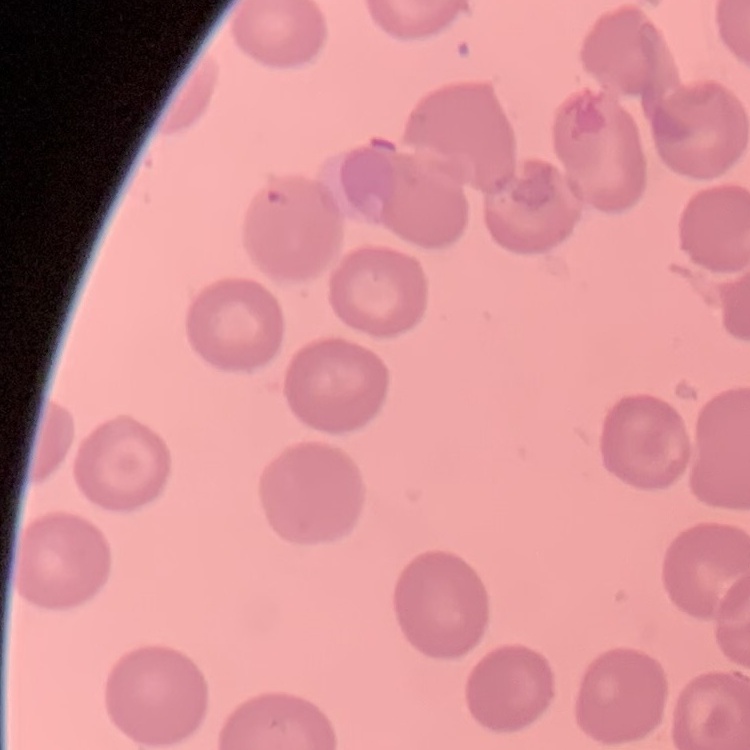
The red blood cells exhibit no rouleaux formation. Field's or Giemsa stain. Square crop of a larger photomicrograph. Thin peripheral smear.